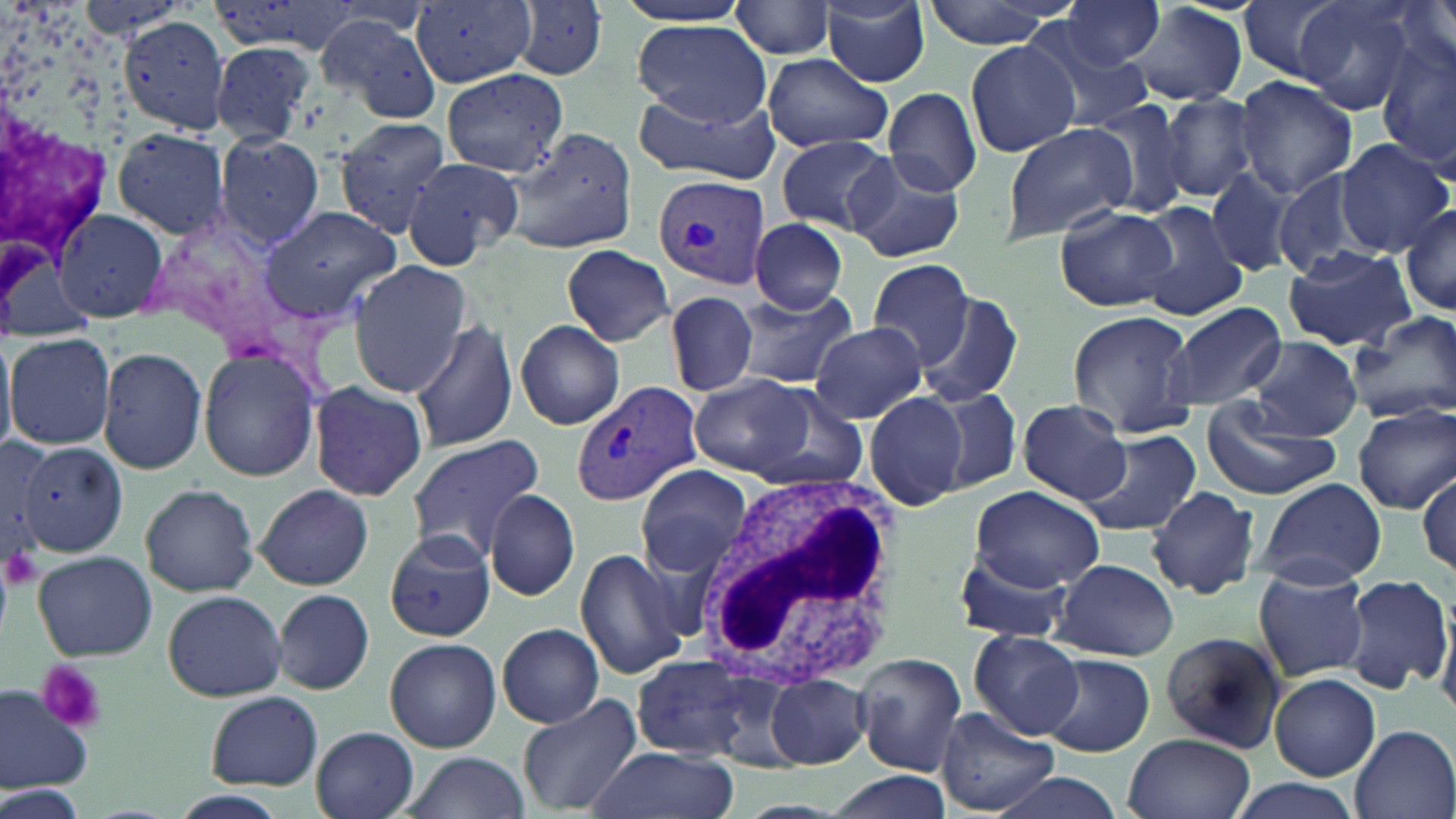
Summary:
  - Coordinate format: approximate bounding boxes as named x1/y1/x2/y2 corners in pixels
  - Platelet locations: (x1=2, y1=542, x2=42, y2=590), (x1=35, y1=661, x2=108, y2=732)
  - Plasmodium vivax-infected red blood cell locations: (x1=654, y1=176, x2=771, y2=292), (x1=572, y1=379, x2=701, y2=509)
  - White blood cell locations: (x1=693, y1=466, x2=900, y2=685)
  - Uninfected red blood cell locations: (x1=205, y1=0, x2=362, y2=59), (x1=1059, y1=0, x2=1163, y2=70), (x1=1236, y1=0, x2=1351, y2=83), (x1=1296, y1=0, x2=1423, y2=112), (x1=612, y1=1, x2=754, y2=27), (x1=821, y1=1, x2=931, y2=86), (x1=924, y1=1, x2=1066, y2=48), (x1=411, y1=2, x2=539, y2=89), (x1=510, y1=2, x2=611, y2=81), (x1=730, y1=2, x2=836, y2=59), (x1=1394, y1=2, x2=1454, y2=71), (x1=1124, y1=4, x2=1247, y2=107), (x1=315, y1=13, x2=442, y2=122), (x1=117, y1=17, x2=229, y2=134), (x1=1020, y1=17, x2=1157, y2=129), (x1=634, y1=20, x2=772, y2=125), (x1=1377, y1=33, x2=1456, y2=173), (x1=965, y1=40, x2=1080, y2=157), (x1=209, y1=41, x2=318, y2=145), (x1=764, y1=53, x2=894, y2=152), (x1=442, y1=69, x2=569, y2=177), (x1=1234, y1=76, x2=1357, y2=201), (x1=633, y1=86, x2=782, y2=186), (x1=883, y1=86, x2=981, y2=196), (x1=1160, y1=93, x2=1257, y2=203), (x1=1090, y1=98, x2=1194, y2=219), (x1=332, y1=117, x2=452, y2=236), (x1=1002, y1=122, x2=1136, y2=242), (x1=111, y1=127, x2=229, y2=240), (x1=504, y1=128, x2=636, y2=255), (x1=214, y1=133, x2=325, y2=248), (x1=775, y1=135, x2=895, y2=233), (x1=1335, y1=139, x2=1451, y2=255), (x1=843, y1=152, x2=964, y2=261), (x1=400, y1=157, x2=524, y2=270), (x1=1204, y1=168, x2=1299, y2=278), (x1=1274, y1=170, x2=1374, y2=278), (x1=1133, y1=201, x2=1247, y2=319), (x1=1400, y1=202, x2=1456, y2=315), (x1=1054, y1=203, x2=1176, y2=311), (x1=257, y1=204, x2=403, y2=323), (x1=53, y1=207, x2=170, y2=324), (x1=748, y1=219, x2=850, y2=315), (x1=561, y1=245, x2=674, y2=346), (x1=1282, y1=247, x2=1417, y2=350), (x1=867, y1=259, x2=978, y2=369), (x1=348, y1=261, x2=474, y2=396), (x1=666, y1=290, x2=758, y2=397), (x1=732, y1=290, x2=859, y2=390), (x1=917, y1=292, x2=1023, y2=407), (x1=1163, y1=301, x2=1285, y2=411), (x1=1067, y1=310, x2=1198, y2=434), (x1=1346, y1=312, x2=1456, y2=423), (x1=408, y1=317, x2=518, y2=452), (x1=516, y1=320, x2=625, y2=430), (x1=810, y1=321, x2=925, y2=425), (x1=0, y1=329, x2=17, y2=459), (x1=6, y1=330, x2=116, y2=451), (x1=1248, y1=337, x2=1362, y2=440), (x1=97, y1=346, x2=208, y2=475), (x1=198, y1=350, x2=321, y2=481), (x1=691, y1=374, x2=815, y2=476), (x1=307, y1=380, x2=428, y2=502), (x1=749, y1=385, x2=870, y2=493), (x1=863, y1=389, x2=970, y2=511), (x1=935, y1=389, x2=1022, y2=490), (x1=1018, y1=400, x2=1131, y2=504), (x1=1202, y1=401, x2=1340, y2=501), (x1=1352, y1=403, x2=1456, y2=514), (x1=998, y1=404, x2=1125, y2=583), (x1=1078, y1=430, x2=1202, y2=539), (x1=405, y1=436, x2=547, y2=560), (x1=0, y1=440, x2=57, y2=571), (x1=17, y1=442, x2=129, y2=558), (x1=636, y1=465, x2=752, y2=580), (x1=1416, y1=471, x2=1455, y2=582), (x1=1255, y1=478, x2=1387, y2=588), (x1=140, y1=484, x2=260, y2=597), (x1=255, y1=484, x2=373, y2=589), (x1=971, y1=485, x2=1103, y2=589), (x1=1148, y1=486, x2=1261, y2=601), (x1=486, y1=489, x2=578, y2=600), (x1=382, y1=528, x2=498, y2=643), (x1=574, y1=548, x2=690, y2=682), (x1=33, y1=549, x2=156, y2=660), (x1=947, y1=549, x2=1075, y2=644), (x1=1053, y1=558, x2=1178, y2=660), (x1=1252, y1=566, x2=1371, y2=682), (x1=1341, y1=573, x2=1452, y2=695), (x1=274, y1=588, x2=374, y2=694), (x1=161, y1=589, x2=287, y2=701), (x1=1434, y1=596, x2=1456, y2=717), (x1=497, y1=623, x2=604, y2=727), (x1=970, y1=630, x2=1083, y2=740), (x1=1157, y1=632, x2=1290, y2=753), (x1=384, y1=637, x2=501, y2=752), (x1=855, y1=653, x2=967, y2=775), (x1=1041, y1=653, x2=1154, y2=758), (x1=630, y1=654, x2=770, y2=759), (x1=1269, y1=673, x2=1381, y2=781), (x1=766, y1=674, x2=870, y2=767), (x1=0, y1=683, x2=93, y2=791), (x1=204, y1=691, x2=324, y2=790), (x1=516, y1=693, x2=644, y2=815), (x1=937, y1=706, x2=1056, y2=816), (x1=1350, y1=725, x2=1455, y2=819), (x1=312, y1=727, x2=420, y2=819), (x1=1124, y1=733, x2=1256, y2=819), (x1=585, y1=747, x2=735, y2=819), (x1=402, y1=753, x2=527, y2=818), (x1=825, y1=770, x2=951, y2=819), (x1=985, y1=772, x2=1131, y2=819), (x1=1223, y1=777, x2=1366, y2=819), (x1=3, y1=779, x2=90, y2=819), (x1=170, y1=790, x2=289, y2=818)
  - Slide-level diagnosis: Plasmodium vivax
  - Stain: May-Grünwald-Giemsa
  - Image size: 1456×819 pixels
  - Magnification: 1000x
  - Field of view: single
  - Preparation: thin blood smear
  - Modality: optical microscopy